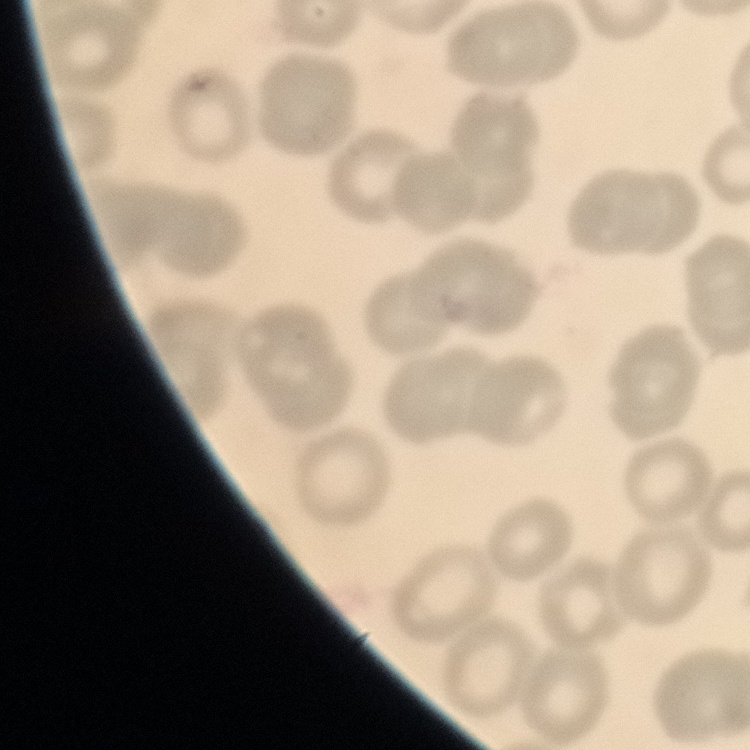
red blood cell morphology = no rouleaux formation
image type = one tile cut from a larger photomicrograph
preparation = thin peripheral smear
stain = Field's or Giemsa